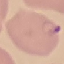
Summary:
  - Malaria status: parasitized
  - Stain: Giemsa
  - Image type: automatically extracted cell patch, resized to 64 × 64 pixels
  - Capture: smartphone through the microscope eyepiece
  - Preparation: thin blood film